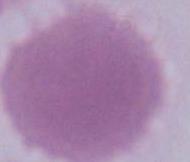
Summary:
  - Modality: micrograph
  - Magnification: 1000x
  - Identification: erythrocyte